Identify the preparation type.
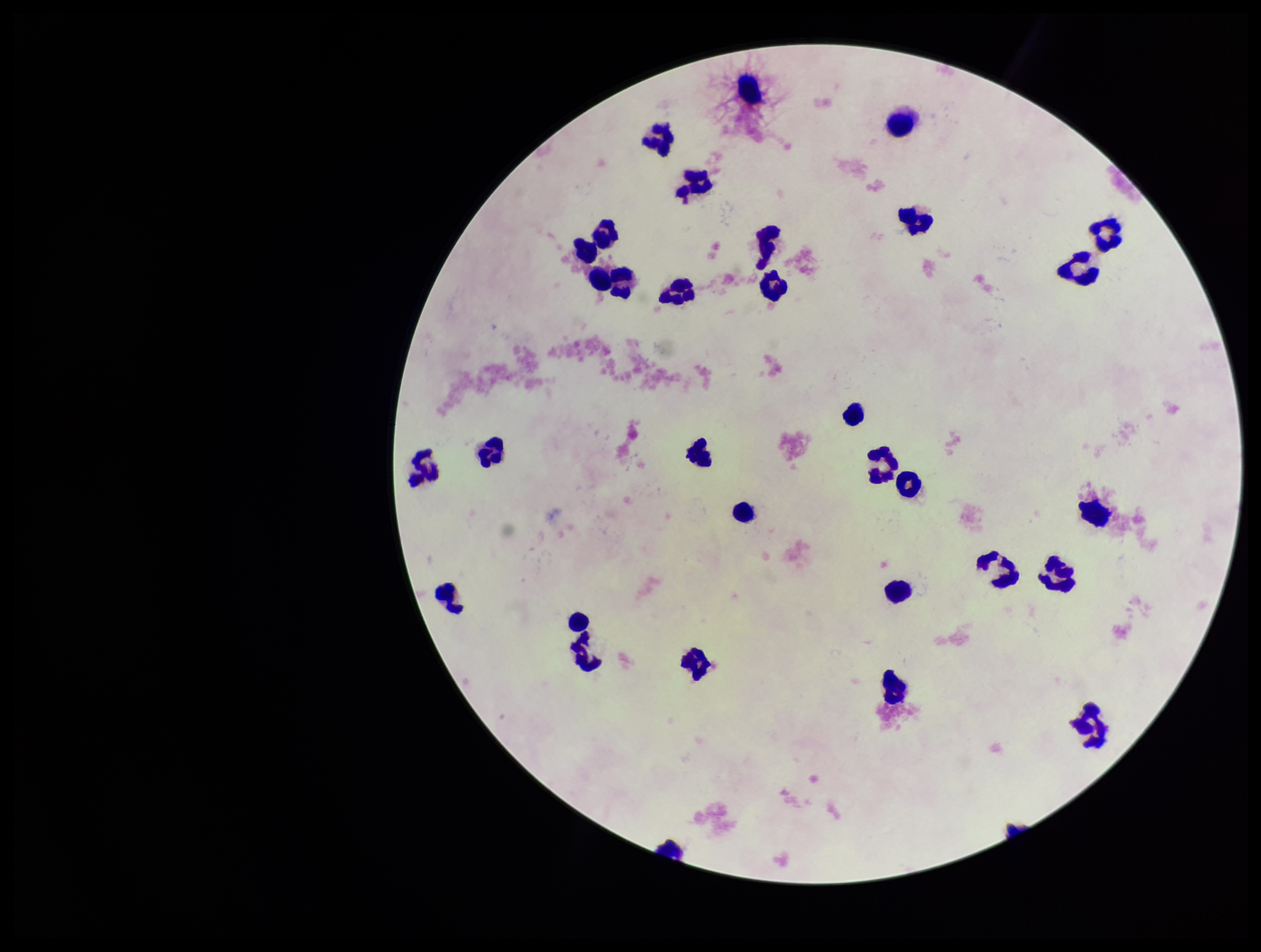
Thick.

Parasite count: 0. Plasmodium parasites: none detected. Leukocyte count: 31. Image is 1261×952 pixels. Patient malaria status: negative. Photographed through the microscope eyepiece with a smartphone camera. Giemsa stain. One field from this slide.